Describe the morphology of the red blood cells.
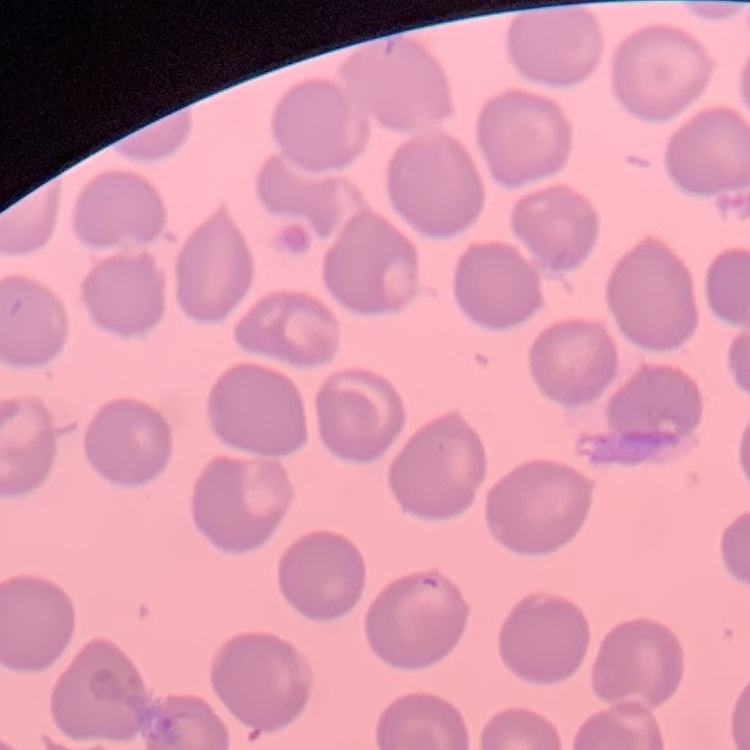

No rouleaux formation.

Summary:
  - Stain: Field's or Giemsa
  - Preparation: thin peripheral smear
  - Image type: square crop of a larger photomicrograph